Classify this cell by malaria status.
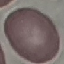
It is uninfected.

Giemsa stain. Acquired by smartphone through the microscope eyepiece. Thin blood film. Automatically extracted cell patch, resized to 64 × 64 pixels.